Assess this cell for malaria.
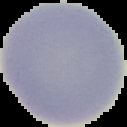
Uninfected.

{
  "preparation": "thin blood smear",
  "image_type": "segmented cell region on a black background",
  "image_size": "127×127 pixels"
}